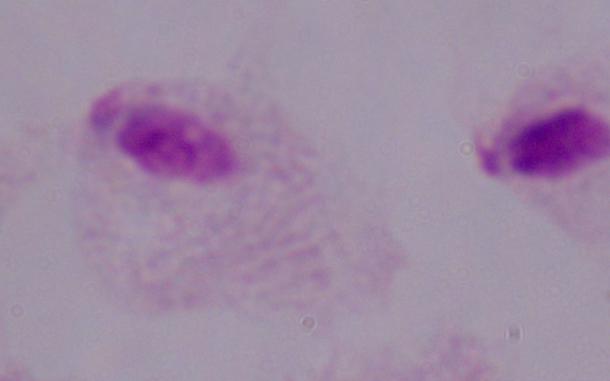

Summary:
  - Modality: micrograph
  - Magnification: 1000x
  - Identification: trichomonad